Give the position of every Plasmodium parasite visible.
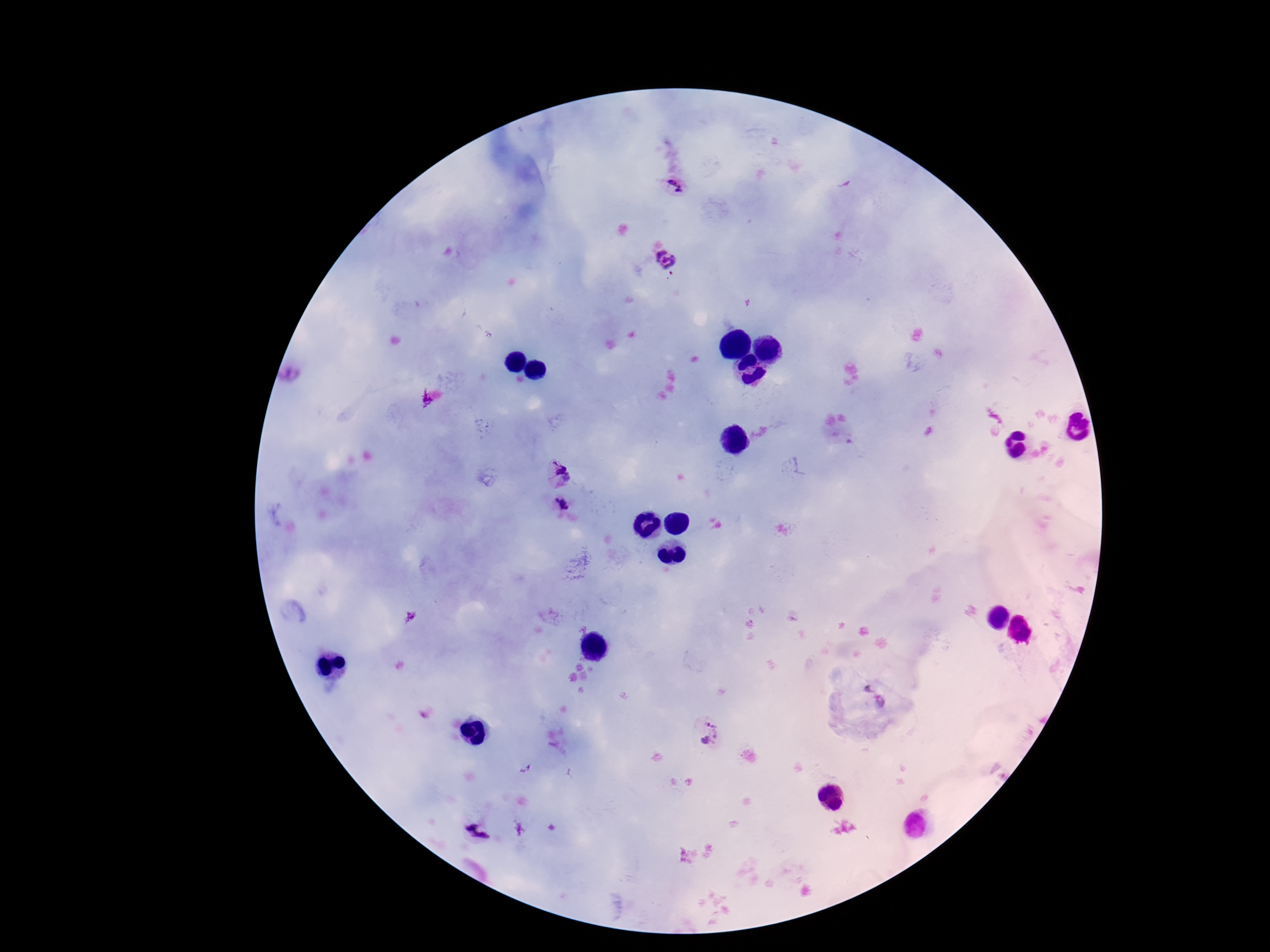
Approximate centers as [x, y] in pixels.
Plasmodium parasites: [675, 184], [668, 258], [556, 473], [562, 503], [866, 688], [880, 703], [701, 729].

Image is 1270×952 pixels. 100x magnification. Thick peripheral-blood smear. Photographed through the microscope eyepiece with a smartphone camera. Patient malaria status: infected. One field from this slide. Giemsa stain.